Classify this cell by malaria status.
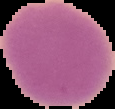
It is uninfected.

Summary:
  - Preparation: thin blood film
  - Image size: 115×109 pixels
  - Image type: segmented cell region on a black background